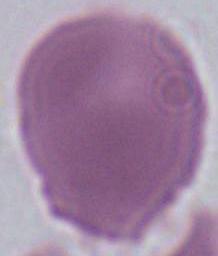

{
  "magnification": "1000x",
  "modality": "micrograph",
  "identification": "red blood cell"
}